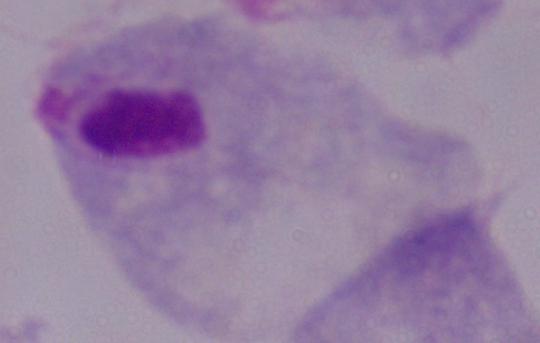
Summary:
  - Magnification: 1000x
  - Modality: photomicrograph
  - Identification: trichomonad